Report the malaria status of this cell.
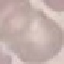

Uninfected.

Summary:
  - Capture: smartphone through the microscope eyepiece
  - Image type: automatically extracted cell patch, resized to 64 × 64 pixels
  - Stain: Giemsa
  - Preparation: thin smear